Which red blood cells are P. falciparum-infected, and which are of indeterminate infection status?
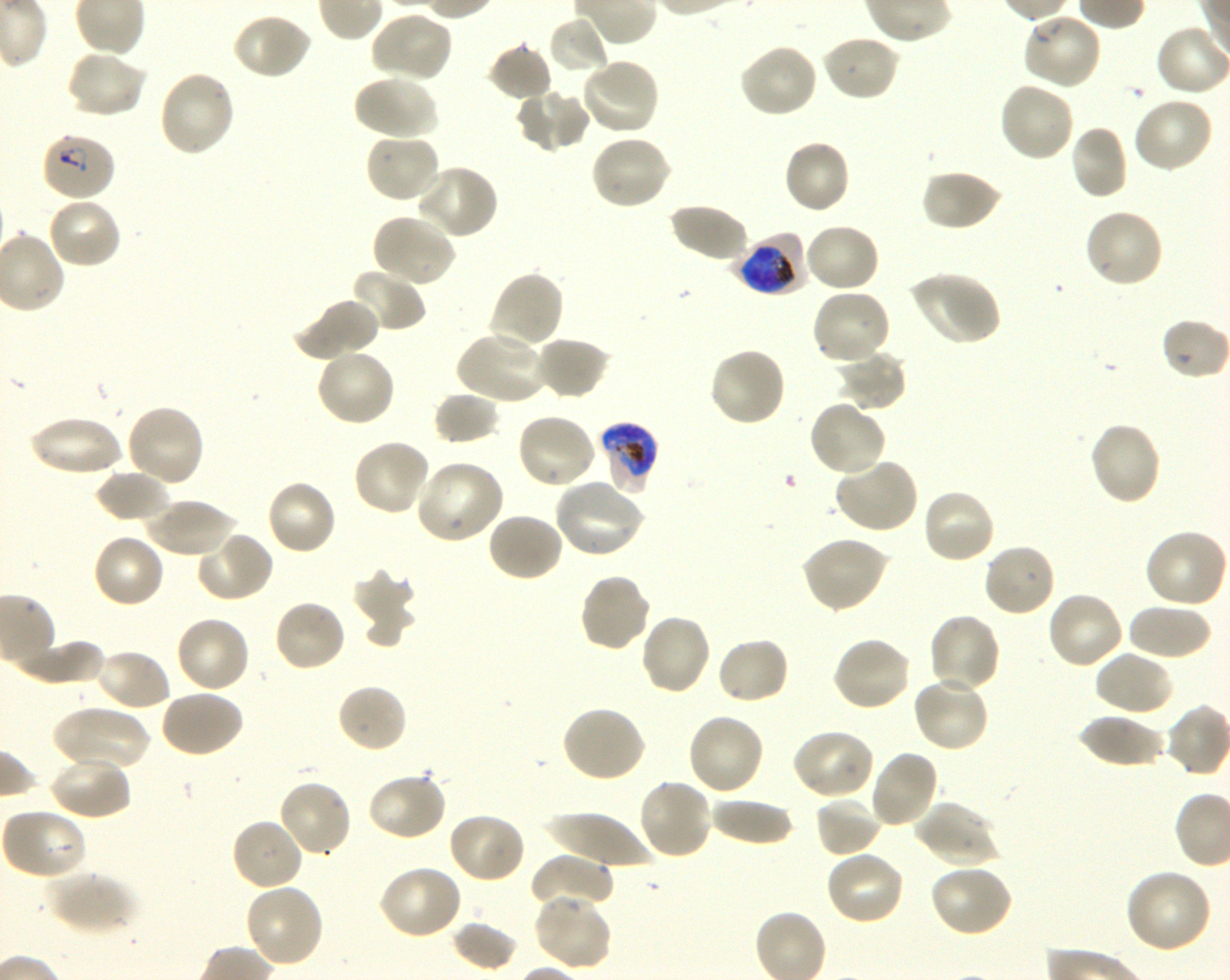
Approximate bounding rectangles given as corner coordinates in pixels from the top-left. Not every red blood cell is marked. A life-cycle stage — or a range of stages, where the recorded stages span more than one — follows each staged infected red blood cell.
Infected red blood cells: (x1=40, y1=132, x2=117, y2=202) ring; (x1=734, y1=233, x2=809, y2=296) early trophozoite to early schizont; (x1=597, y1=421, x2=660, y2=495) early trophozoite to late schizont.
No red blood cells of indeterminate infection status observed.

locations_of_uninfected_red_blood_cells: (x1=370, y1=10, x2=453, y2=83), (x1=232, y1=12, x2=312, y2=80), (x1=1021, y1=13, x2=1102, y2=91), (x1=548, y1=17, x2=608, y2=75), (x1=820, y1=34, x2=901, y2=102), (x1=738, y1=42, x2=819, y2=119), (x1=486, y1=43, x2=554, y2=101), (x1=66, y1=48, x2=147, y2=118), (x1=579, y1=59, x2=661, y2=137), (x1=157, y1=69, x2=236, y2=158), (x1=352, y1=74, x2=438, y2=141), (x1=998, y1=80, x2=1075, y2=163), (x1=514, y1=88, x2=590, y2=153), (x1=1131, y1=96, x2=1213, y2=175), (x1=1068, y1=125, x2=1128, y2=200), (x1=364, y1=132, x2=442, y2=205), (x1=589, y1=133, x2=672, y2=211), (x1=782, y1=138, x2=852, y2=215), (x1=414, y1=162, x2=499, y2=240), (x1=920, y1=169, x2=1004, y2=233), (x1=46, y1=195, x2=123, y2=270), (x1=668, y1=202, x2=750, y2=265), (x1=1083, y1=208, x2=1164, y2=290), (x1=371, y1=212, x2=457, y2=287), (x1=804, y1=222, x2=881, y2=294), (x1=349, y1=268, x2=426, y2=333), (x1=488, y1=269, x2=564, y2=351), (x1=908, y1=270, x2=1000, y2=346), (x1=811, y1=289, x2=891, y2=368), (x1=293, y1=296, x2=380, y2=361), (x1=1162, y1=318, x2=1228, y2=380), (x1=455, y1=329, x2=547, y2=406), (x1=532, y1=336, x2=611, y2=400), (x1=708, y1=346, x2=787, y2=428), (x1=315, y1=348, x2=397, y2=427), (x1=837, y1=349, x2=908, y2=412), (x1=433, y1=390, x2=502, y2=445), (x1=808, y1=399, x2=888, y2=477), (x1=124, y1=403, x2=206, y2=488), (x1=515, y1=412, x2=598, y2=490), (x1=27, y1=416, x2=126, y2=478), (x1=1087, y1=421, x2=1163, y2=507), (x1=352, y1=438, x2=431, y2=516), (x1=835, y1=456, x2=920, y2=534), (x1=413, y1=459, x2=505, y2=545), (x1=94, y1=467, x2=172, y2=524), (x1=265, y1=478, x2=337, y2=556), (x1=553, y1=479, x2=645, y2=559), (x1=920, y1=487, x2=996, y2=566), (x1=144, y1=498, x2=238, y2=557), (x1=485, y1=511, x2=565, y2=583), (x1=1142, y1=529, x2=1227, y2=609), (x1=195, y1=531, x2=275, y2=604), (x1=92, y1=533, x2=166, y2=610), (x1=800, y1=535, x2=890, y2=613), (x1=981, y1=543, x2=1056, y2=618), (x1=351, y1=569, x2=417, y2=643), (x1=578, y1=572, x2=652, y2=653), (x1=1046, y1=591, x2=1124, y2=671), (x1=272, y1=598, x2=347, y2=673), (x1=1127, y1=603, x2=1212, y2=660), (x1=638, y1=612, x2=712, y2=696), (x1=927, y1=612, x2=1002, y2=692), (x1=174, y1=615, x2=250, y2=694), (x1=831, y1=635, x2=913, y2=712), (x1=716, y1=637, x2=790, y2=705), (x1=9, y1=638, x2=105, y2=685), (x1=93, y1=647, x2=172, y2=713), (x1=1093, y1=650, x2=1174, y2=718), (x1=911, y1=674, x2=990, y2=754), (x1=336, y1=682, x2=408, y2=754), (x1=158, y1=688, x2=244, y2=758), (x1=53, y1=705, x2=151, y2=773), (x1=560, y1=705, x2=647, y2=785), (x1=687, y1=712, x2=766, y2=796), (x1=1077, y1=714, x2=1166, y2=769), (x1=790, y1=728, x2=876, y2=801), (x1=868, y1=748, x2=940, y2=830), (x1=49, y1=755, x2=132, y2=820), (x1=366, y1=770, x2=447, y2=843), (x1=636, y1=777, x2=713, y2=861), (x1=276, y1=779, x2=353, y2=858), (x1=815, y1=796, x2=882, y2=858), (x1=707, y1=797, x2=794, y2=846), (x1=914, y1=799, x2=1001, y2=868), (x1=2, y1=809, x2=91, y2=879), (x1=446, y1=811, x2=526, y2=884), (x1=545, y1=811, x2=656, y2=869), (x1=230, y1=818, x2=304, y2=892), (x1=824, y1=849, x2=906, y2=925), (x1=530, y1=854, x2=614, y2=914), (x1=928, y1=863, x2=1015, y2=939), (x1=377, y1=865, x2=464, y2=941), (x1=1125, y1=867, x2=1213, y2=954), (x1=46, y1=869, x2=137, y2=935), (x1=244, y1=883, x2=325, y2=968), (x1=532, y1=893, x2=613, y2=972), (x1=451, y1=920, x2=519, y2=972)
donor_blood_group: O+
culture: shaking in-vitro P. falciparum strain 3D7
preparation: thin blood smear
stain: Giemsa
image_size: 1230×980 pixels
objective: 100x, oil immersion, numerical aperture 1.30
field_of_view: one from this slide